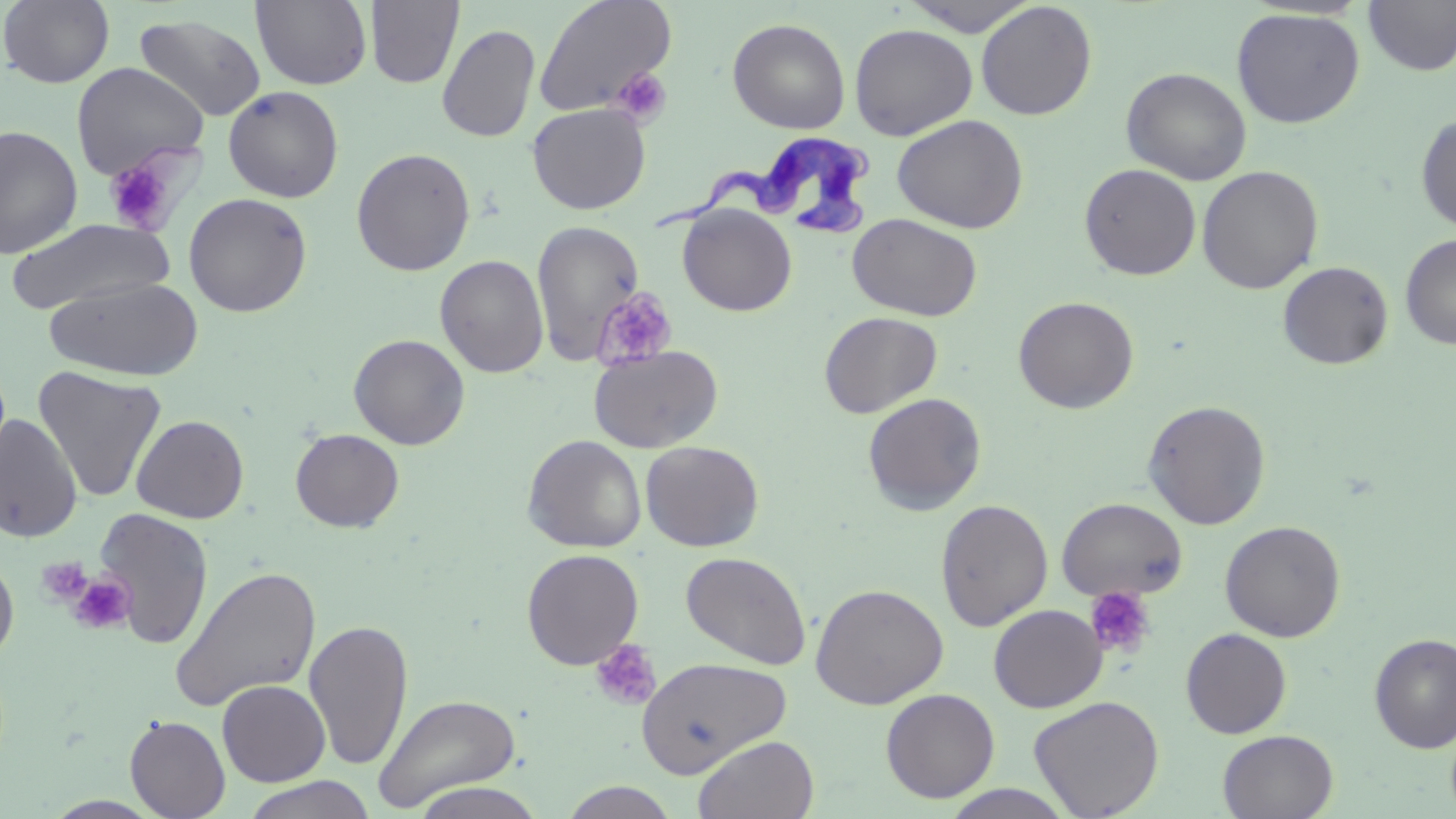 Approximate bounding boxes as [x1, y1, x2, y2] in pixels. Trypanosoma brucei locations: [648, 136, 882, 239]. Uninfected red blood cell locations: [0, 0, 115, 88], [251, 0, 372, 90], [365, 0, 463, 88], [533, 0, 677, 118], [900, 0, 1042, 37], [1363, 0, 1456, 76], [976, 1, 1097, 121], [1231, 7, 1366, 129], [135, 13, 266, 122], [727, 17, 851, 134], [849, 23, 977, 140], [437, 24, 540, 143], [71, 61, 208, 179], [1120, 67, 1252, 185], [223, 86, 344, 202], [527, 103, 651, 215], [1415, 112, 1456, 233], [892, 114, 1029, 233], [0, 125, 83, 260], [351, 148, 475, 276], [1079, 163, 1201, 280], [1197, 165, 1324, 294], [183, 192, 312, 317], [678, 204, 797, 316], [848, 213, 983, 322], [7, 218, 173, 315], [532, 219, 645, 364], [1399, 232, 1456, 351], [435, 254, 549, 378], [1278, 261, 1393, 370], [44, 276, 204, 381], [1013, 296, 1139, 414], [818, 311, 943, 418], [349, 334, 470, 450], [589, 344, 723, 453], [33, 366, 167, 503], [863, 392, 987, 515], [1142, 400, 1271, 529], [0, 414, 82, 543], [131, 414, 249, 523], [290, 428, 404, 532], [522, 434, 647, 553], [641, 440, 765, 551], [1056, 496, 1188, 603], [935, 498, 1053, 632], [92, 507, 214, 650], [1220, 521, 1346, 642], [521, 548, 644, 669], [681, 550, 812, 670], [0, 553, 19, 667], [169, 564, 321, 713], [810, 583, 948, 710], [989, 604, 1107, 712], [304, 619, 414, 771], [1180, 628, 1291, 739], [1370, 633, 1456, 753], [587, 639, 663, 710], [636, 655, 791, 777], [217, 679, 331, 786], [880, 688, 1000, 803], [372, 692, 523, 812], [1029, 695, 1165, 818], [124, 715, 231, 819], [1218, 729, 1339, 819], [693, 734, 819, 819], [241, 775, 376, 819], [409, 781, 548, 819], [559, 781, 680, 819], [939, 785, 1079, 819]. Platelet locations: [609, 67, 673, 127], [102, 155, 178, 234], [592, 286, 677, 370], [37, 557, 92, 606], [68, 574, 135, 634], [1084, 587, 1156, 661], [590, 640, 662, 711]. Slide-level diagnosis: Trypanosoma brucei. Single field of view. Captured at 1000x magnification. May-Grünwald-Giemsa-stained preparation. Thin blood smear. Optical microscopy. Image is 1456×819 pixels.